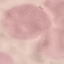

Result: negative for malaria parasites. Acquired by smartphone through the microscope eyepiece. Thin blood smear. Giemsa stain. Cell patch, automatically extracted from a larger field of view and resized to 64 × 64 pixels.